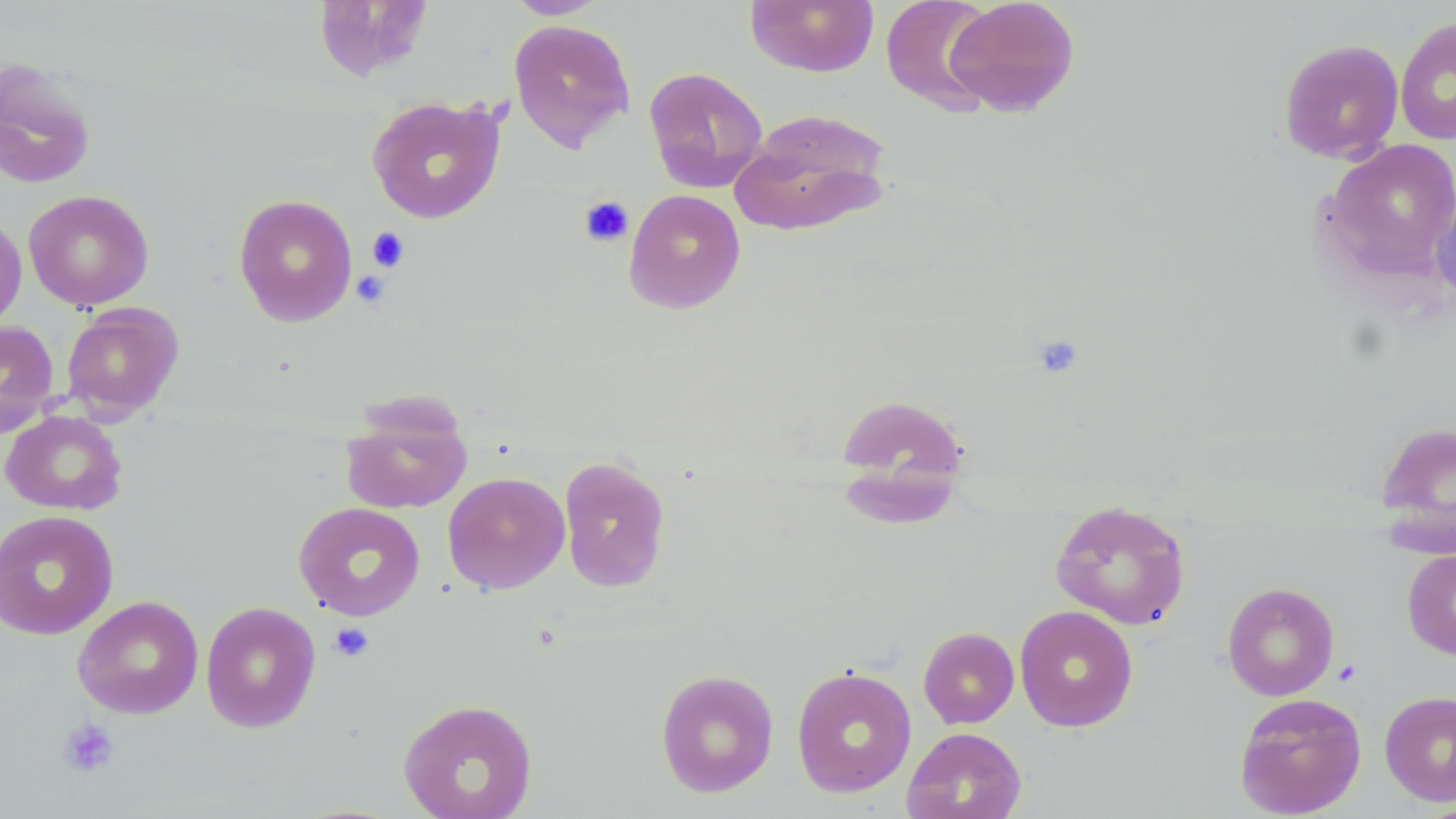

Summary:
  - Coordinate format: approximate bounding boxes as (x1, y1, x2, y2) in pixels
  - Uninfected red blood cell locations: (505, 0, 608, 19), (744, 0, 879, 77), (880, 0, 998, 115), (944, 0, 1081, 117), (1395, 16, 1456, 145), (508, 18, 635, 152), (1278, 38, 1404, 163), (0, 58, 96, 189), (643, 66, 769, 193), (366, 96, 506, 224), (731, 108, 893, 236), (1322, 139, 1456, 282), (1432, 183, 1456, 307), (623, 188, 746, 314), (23, 189, 154, 311), (233, 194, 358, 326), (0, 211, 27, 332), (61, 303, 184, 419), (0, 320, 59, 437), (833, 391, 969, 522), (340, 404, 472, 514), (1, 409, 127, 515), (1374, 418, 1456, 554), (558, 456, 671, 593), (442, 471, 570, 595), (1050, 498, 1191, 630), (293, 501, 426, 621), (0, 509, 118, 640), (1401, 548, 1456, 660), (1223, 581, 1340, 701), (72, 595, 204, 718), (200, 601, 322, 733), (1014, 605, 1139, 732), (918, 626, 1019, 728), (791, 665, 917, 797), (655, 668, 779, 798), (1380, 690, 1456, 807), (1234, 692, 1367, 818), (398, 698, 538, 819), (902, 727, 1027, 819)
  - Platelet locations: (579, 195, 634, 247), (366, 227, 410, 272), (351, 269, 392, 308), (1031, 333, 1084, 379), (329, 622, 374, 663), (58, 718, 120, 779)
  - Slide-level diagnosis: no evidence of blood parasites
  - Modality: light microscopy
  - Image size: 1456×819 pixels
  - Stain: May-Grünwald-Giemsa
  - Preparation: thin blood smear
  - Field of view: single
  - Magnification: 1000x